Point out each Plasmodium parasite.
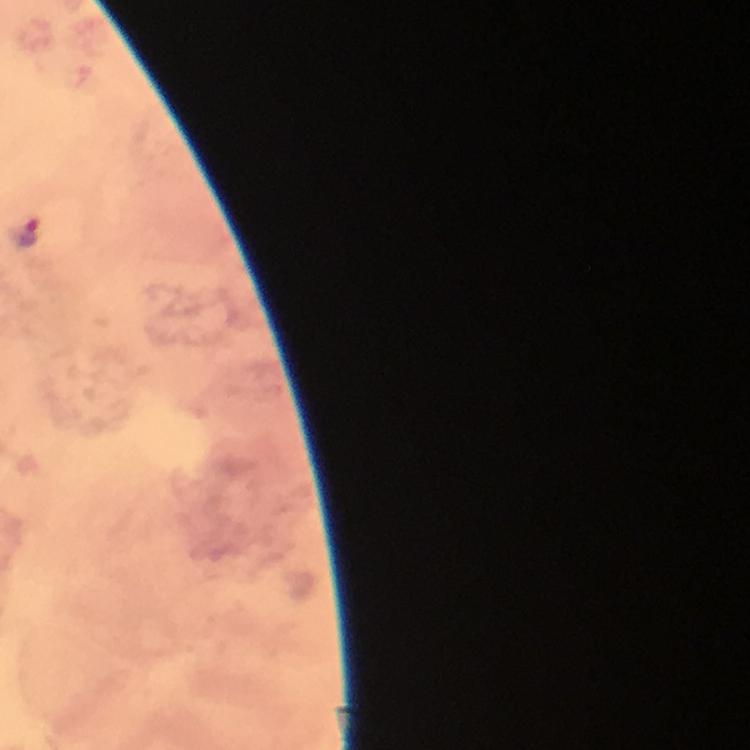
Approximate centers as [x, y] in pixels.
Plasmodium parasites: [28, 233].

stain: Giemsa
cropped_from: one field of view
magnification: 100x
preparation: thick smear
context: from a malaria diagnostic workup
immersion_oil: used
image_size: 750×750 pixels
capture: smartphone photograph through a microscope